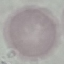

Summary:
  - Result: no malaria parasites seen
  - Image type: automatically extracted cell patch, resized to 64 × 64 pixels
  - Preparation: thin smear
  - Capture: smartphone camera at the microscope eyepiece
  - Stain: Giemsa